Locate and identify every blood parasite.
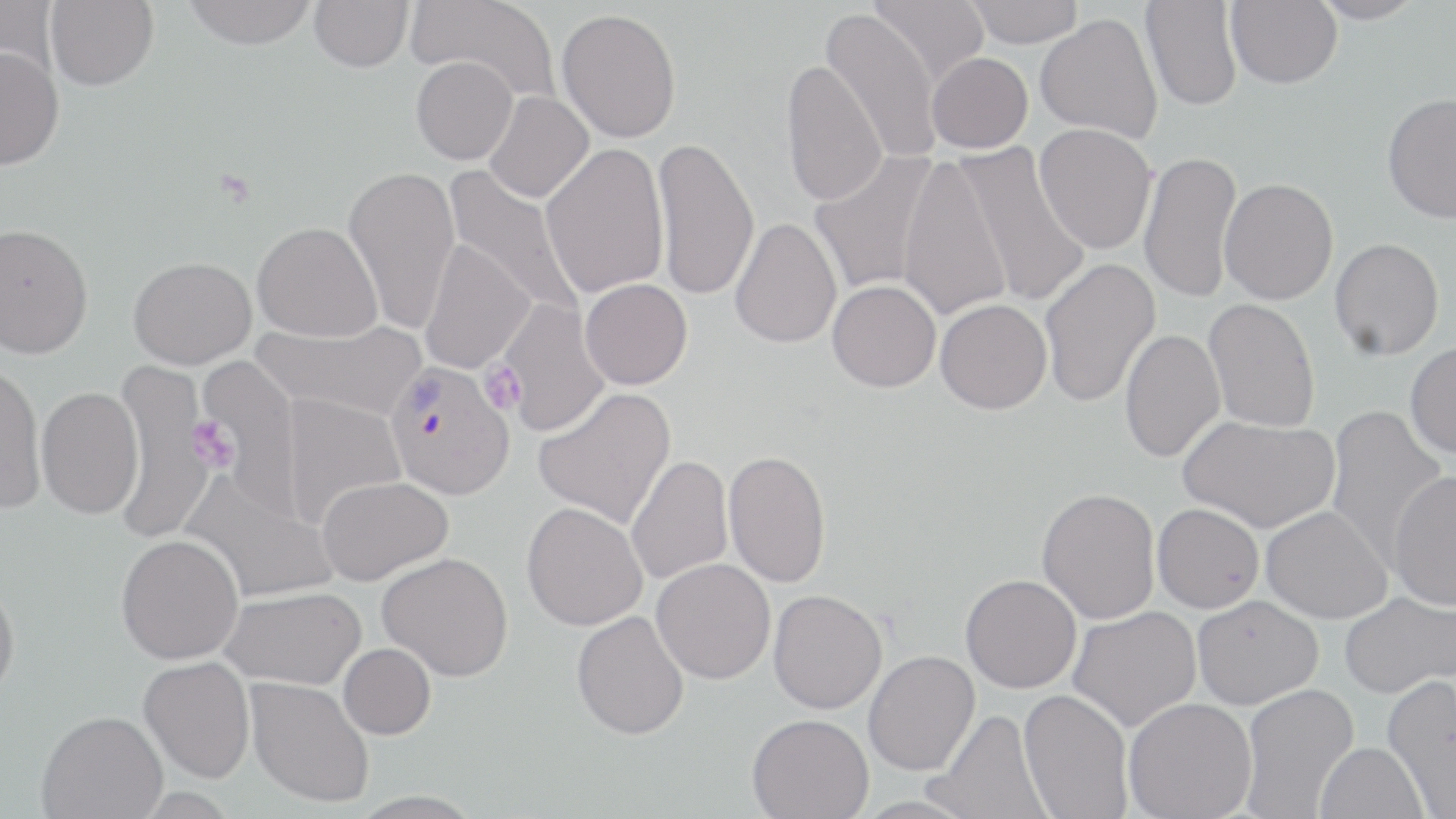
Approximate bounding boxes as named x1/y1/x2/y2 corners in pixels.
Plasmodium vivax-infected red blood cells: (x1=391, y1=358, x2=521, y2=497).
No Plasmodium falciparum, Plasmodium ovale, Plasmodium malariae, Babesia divergens, or Trypanosoma brucei observed.

Summary:
  - Uninfected red blood cell locations: (x1=45, y1=0, x2=159, y2=91), (x1=183, y1=0, x2=317, y2=50), (x1=308, y1=0, x2=413, y2=72), (x1=407, y1=0, x2=562, y2=106), (x1=868, y1=0, x2=990, y2=86), (x1=964, y1=0, x2=1085, y2=48), (x1=1141, y1=0, x2=1242, y2=112), (x1=1225, y1=0, x2=1342, y2=88), (x1=1307, y1=0, x2=1425, y2=24), (x1=0, y1=1, x2=59, y2=85), (x1=557, y1=8, x2=681, y2=143), (x1=821, y1=8, x2=943, y2=164), (x1=1035, y1=12, x2=1163, y2=143), (x1=0, y1=46, x2=64, y2=170), (x1=927, y1=52, x2=1033, y2=153), (x1=411, y1=57, x2=518, y2=165), (x1=780, y1=58, x2=888, y2=207), (x1=484, y1=92, x2=594, y2=203), (x1=1382, y1=93, x2=1456, y2=223), (x1=1034, y1=124, x2=1157, y2=254), (x1=651, y1=135, x2=759, y2=302), (x1=951, y1=141, x2=1092, y2=309), (x1=541, y1=142, x2=669, y2=298), (x1=809, y1=149, x2=941, y2=296), (x1=1139, y1=150, x2=1242, y2=304), (x1=895, y1=154, x2=1012, y2=323), (x1=343, y1=165, x2=461, y2=335), (x1=442, y1=165, x2=584, y2=321), (x1=1220, y1=178, x2=1339, y2=304), (x1=730, y1=217, x2=843, y2=349), (x1=252, y1=221, x2=382, y2=341), (x1=0, y1=223, x2=93, y2=357), (x1=1329, y1=238, x2=1444, y2=360), (x1=419, y1=239, x2=534, y2=374), (x1=129, y1=256, x2=257, y2=369), (x1=1039, y1=257, x2=1160, y2=408), (x1=580, y1=279, x2=693, y2=390), (x1=827, y1=280, x2=941, y2=392), (x1=497, y1=298, x2=610, y2=437), (x1=1203, y1=298, x2=1320, y2=432), (x1=935, y1=299, x2=1052, y2=414), (x1=253, y1=317, x2=427, y2=421), (x1=1119, y1=329, x2=1225, y2=462), (x1=1405, y1=340, x2=1456, y2=459), (x1=194, y1=355, x2=303, y2=512), (x1=109, y1=360, x2=219, y2=543), (x1=0, y1=361, x2=47, y2=514), (x1=36, y1=385, x2=144, y2=519), (x1=533, y1=386, x2=676, y2=530), (x1=278, y1=393, x2=406, y2=527), (x1=1323, y1=406, x2=1449, y2=567), (x1=1179, y1=416, x2=1340, y2=533), (x1=723, y1=449, x2=832, y2=588), (x1=626, y1=454, x2=733, y2=585), (x1=1387, y1=470, x2=1456, y2=610), (x1=180, y1=471, x2=339, y2=605), (x1=316, y1=475, x2=454, y2=586), (x1=1037, y1=487, x2=1161, y2=624), (x1=521, y1=502, x2=648, y2=631), (x1=1152, y1=503, x2=1265, y2=613), (x1=1261, y1=505, x2=1392, y2=624), (x1=116, y1=534, x2=244, y2=664), (x1=377, y1=552, x2=513, y2=681), (x1=652, y1=558, x2=776, y2=684), (x1=961, y1=574, x2=1082, y2=693), (x1=0, y1=577, x2=21, y2=703), (x1=220, y1=587, x2=366, y2=689), (x1=768, y1=589, x2=888, y2=713), (x1=1340, y1=590, x2=1455, y2=698), (x1=1192, y1=595, x2=1323, y2=708), (x1=1067, y1=606, x2=1202, y2=731), (x1=571, y1=610, x2=689, y2=740), (x1=339, y1=643, x2=436, y2=739), (x1=863, y1=650, x2=980, y2=775), (x1=138, y1=656, x2=255, y2=783), (x1=1381, y1=674, x2=1456, y2=816), (x1=246, y1=677, x2=374, y2=808), (x1=1240, y1=683, x2=1359, y2=817), (x1=1019, y1=688, x2=1133, y2=819), (x1=1123, y1=697, x2=1257, y2=819), (x1=931, y1=708, x2=1051, y2=818), (x1=37, y1=710, x2=167, y2=818), (x1=747, y1=713, x2=874, y2=819), (x1=1314, y1=741, x2=1428, y2=819)
  - Platelet locations: (x1=481, y1=361, x2=526, y2=415), (x1=189, y1=414, x2=236, y2=473)
  - Slide-level diagnosis: Plasmodium vivax
  - Image size: 1456×819 pixels
  - Modality: optical microscopy
  - Preparation: thin blood film
  - Stain: May-Grünwald-Giemsa
  - Magnification: 1000x
  - Field of view: single